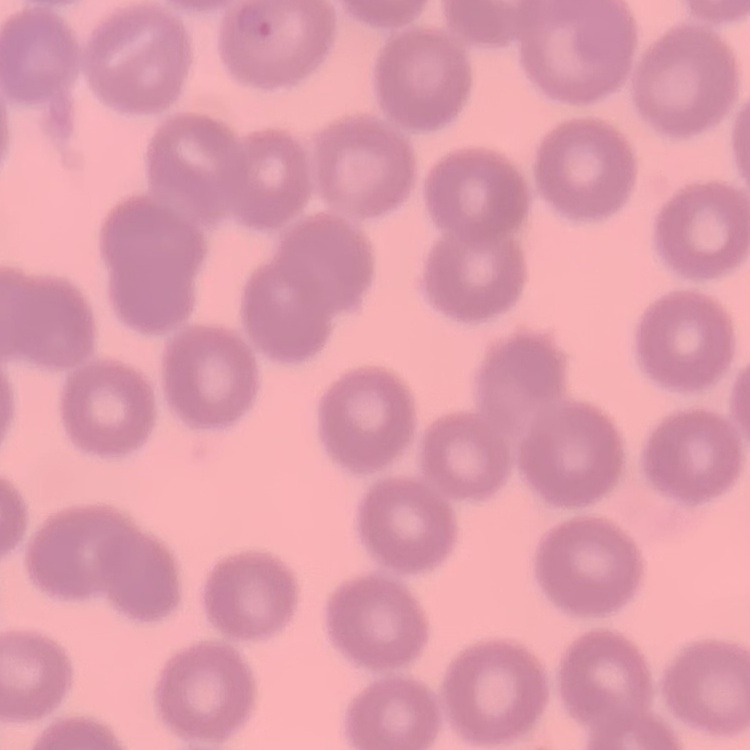

{
  "red_blood_cell_morphology": "no rouleaux formation",
  "preparation": "thin blood smear",
  "stain": "Field's or Giemsa",
  "image_type": "square crop of a larger photomicrograph"
}